Assess the morphology of the erythrocytes.
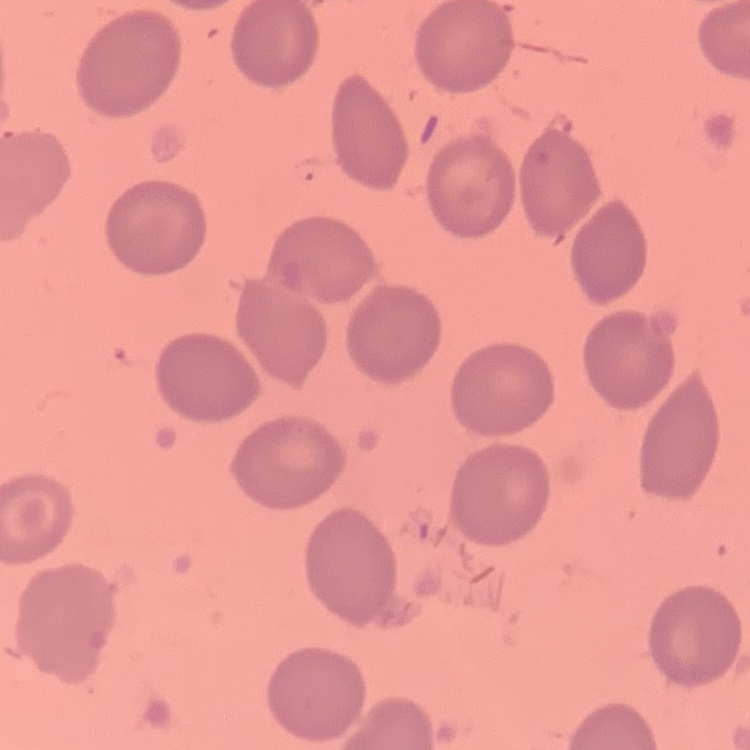
They show no rouleaux formation.

Thin peripheral smear. One tile cut from a larger photomicrograph. Stained with either Field's or Giemsa.